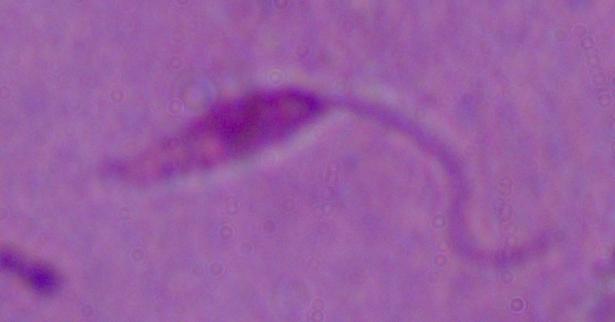
Micrograph. Captured at 1000x magnification. A Leishmania parasite is seen.